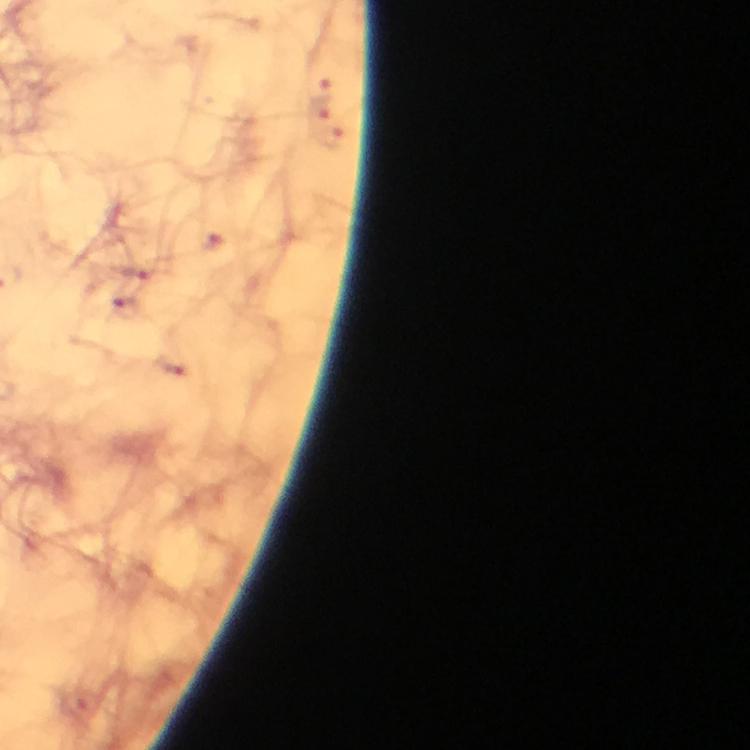

Approximate centers as {x, y} in pixels.
Summary:
  - Malaria parasite locations: {317, 107}, {332, 134}, {220, 251}, {134, 271}, {129, 308}, {173, 368}
  - Magnification: 100x
  - Image size: 750×750 pixels
  - Stain: Giemsa
  - Immersion oil: used
  - Preparation: thick smear
  - Capture: smartphone photograph through a microscope
  - Cropped from: a single field of view
  - Context: from a malaria diagnostic workup